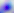

modality = micrograph
magnification = 400x
identification = Toxoplasma gondii